Classify this cell by malaria status.
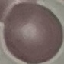
It is uninfected.

Thin blood smear. Giemsa-stained preparation. Photographed with a smartphone camera at the microscope eyepiece. Automatically extracted cell patch, resized to 64 × 64 pixels.